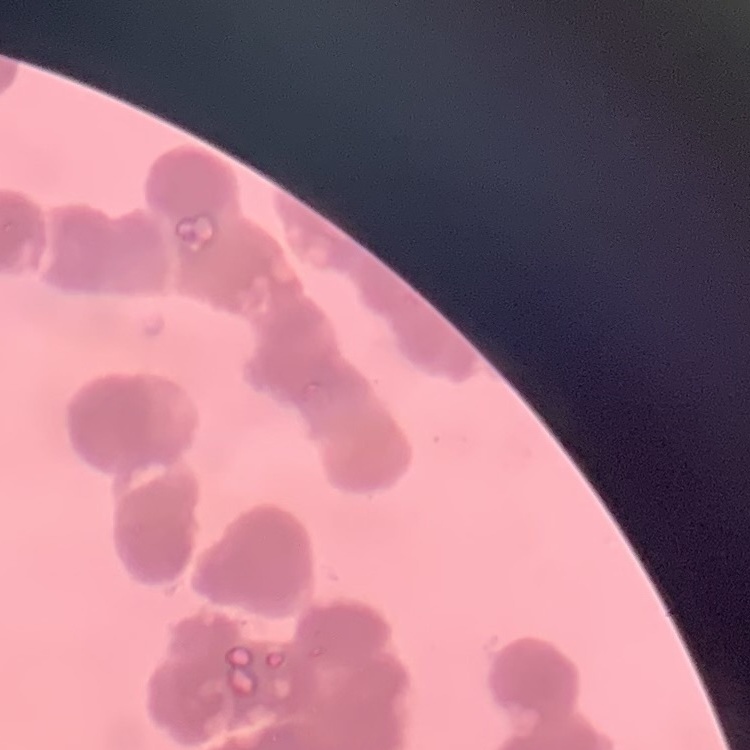

The red blood cells exhibit rouleaux formation. Thin blood smear. One tile cut from a larger photomicrograph. Field's or Giemsa stain.